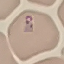

Malaria status: parasitized. Thin blood smear. Giemsa stain. Cell patch, automatically extracted from a larger field of view and resized to 64 × 64 pixels. Acquired by smartphone through the microscope eyepiece.